Locate every blood parasite and identify its species.
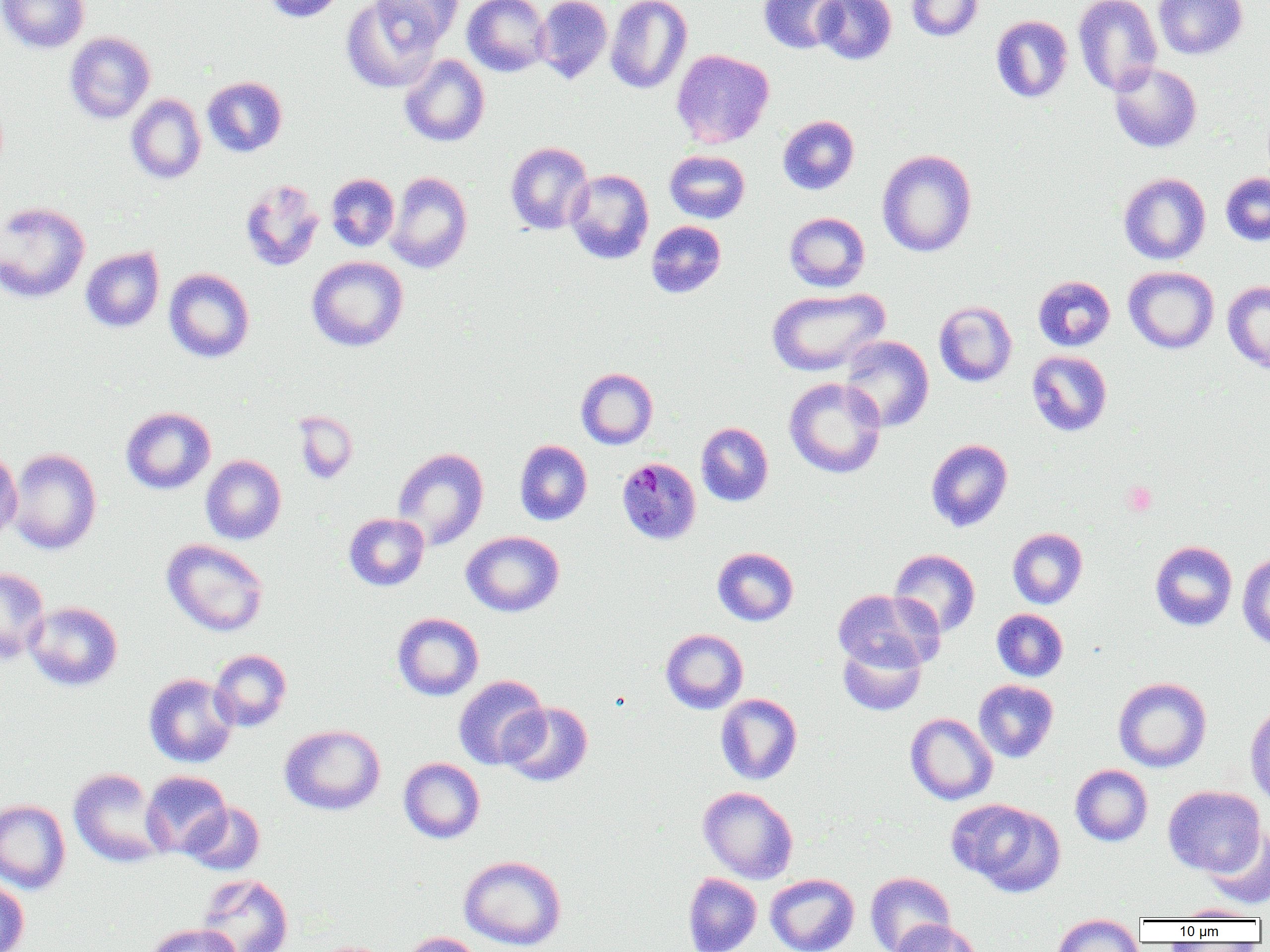
Approximate bounding boxes as (x1, y1, x2, y2) in pixels.
Plasmodium malariae-infected red blood cells: (616, 457, 702, 546).
No Plasmodium falciparum, Plasmodium ovale, Plasmodium vivax, Babesia divergens, or Trypanosoma brucei observed.

Summary:
  - Uninfected red blood cell locations: (0, 0, 89, 54), (261, 0, 347, 23), (342, 0, 440, 93), (373, 0, 463, 50), (463, 0, 551, 77), (534, 0, 613, 84), (758, 0, 847, 54), (814, 0, 896, 65), (905, 0, 983, 41), (1073, 0, 1162, 96), (1153, 0, 1248, 59), (605, 1, 692, 94), (990, 15, 1073, 103), (64, 32, 156, 124), (671, 49, 774, 148), (399, 54, 490, 147), (1109, 62, 1202, 153), (202, 76, 287, 158), (126, 93, 206, 184), (778, 115, 859, 195), (505, 142, 594, 235), (877, 149, 977, 257), (664, 150, 750, 224), (565, 169, 654, 264), (386, 171, 473, 273), (1220, 172, 1270, 246), (326, 173, 400, 252), (1119, 173, 1211, 264), (239, 179, 324, 272), (0, 201, 90, 303), (784, 212, 870, 292), (646, 220, 726, 298), (80, 246, 165, 333), (306, 256, 408, 352), (1123, 266, 1219, 354), (163, 268, 255, 363), (1033, 275, 1115, 352), (1222, 280, 1270, 373), (767, 287, 889, 377), (933, 300, 1017, 387), (839, 336, 934, 432), (1026, 350, 1113, 437), (576, 368, 658, 449), (784, 377, 886, 479), (121, 406, 216, 495), (292, 410, 358, 484), (696, 422, 773, 506), (926, 438, 1013, 532), (515, 439, 592, 525), (392, 447, 489, 550), (0, 448, 22, 544), (6, 448, 102, 555), (200, 455, 286, 545), (344, 513, 430, 591), (1007, 527, 1087, 609), (461, 531, 564, 617), (161, 538, 269, 636), (1150, 540, 1237, 631), (712, 547, 799, 626), (889, 548, 981, 637), (1237, 552, 1270, 650), (0, 567, 50, 665), (832, 588, 944, 673), (25, 601, 123, 691), (992, 609, 1068, 681), (392, 612, 484, 701), (660, 628, 748, 714), (837, 637, 927, 716), (209, 649, 292, 732), (143, 673, 238, 768), (452, 675, 549, 770), (1113, 677, 1212, 772), (973, 679, 1059, 762), (715, 693, 802, 785), (499, 701, 593, 787), (1245, 702, 1270, 810), (905, 713, 997, 805), (279, 724, 385, 816), (398, 757, 485, 843), (1070, 764, 1153, 846), (68, 767, 167, 867), (141, 770, 231, 857), (1163, 785, 1265, 876), (698, 786, 798, 883), (949, 798, 1065, 897), (0, 799, 71, 894), (181, 801, 265, 875), (1204, 826, 1270, 909), (458, 854, 567, 951), (683, 872, 762, 952), (865, 872, 956, 952), (765, 873, 860, 952), (196, 874, 293, 952), (0, 878, 30, 952), (1172, 904, 1263, 921), (1051, 915, 1144, 952), (890, 919, 982, 952), (144, 923, 243, 952), (400, 932, 484, 952), (305, 940, 398, 952)
  - Platelet locations: (1122, 481, 1157, 516)
  - Slide-level diagnosis: Plasmodium malariae
  - Magnification: 1000x
  - Image size: 1270×952 pixels
  - Field of view: one of a larger specimen
  - Modality: light microscopy
  - Preparation: thin blood smear